State which parasite is depicted.
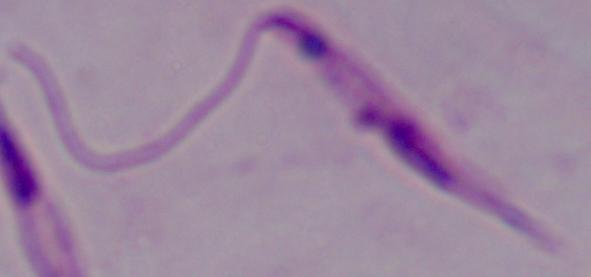
Leishmania.

modality: micrograph
magnification: 1000x